State which cell type is depicted.
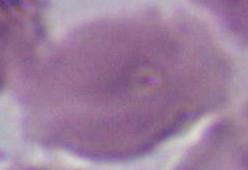

An erythrocyte.

Micrograph. 1000x magnification.